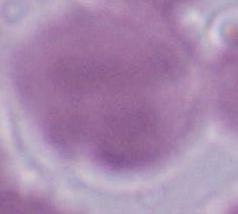
magnification: 1000x
modality: photomicrograph
identification: erythrocyte